Assess this cell for malaria.
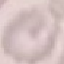
It is uninfected.

Summary:
  - Stain: Giemsa
  - Preparation: thin blood smear
  - Capture: smartphone camera at the microscope eyepiece
  - Image type: cell patch, automatically extracted from a larger field of view and resized to 64 × 64 pixels